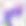

400x magnification. Photomicrograph. Toxoplasma gondii is seen.